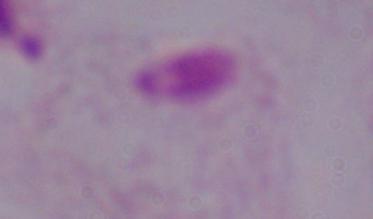

{
  "magnification": "1000x",
  "modality": "micrograph",
  "identification": "trichomonad"
}